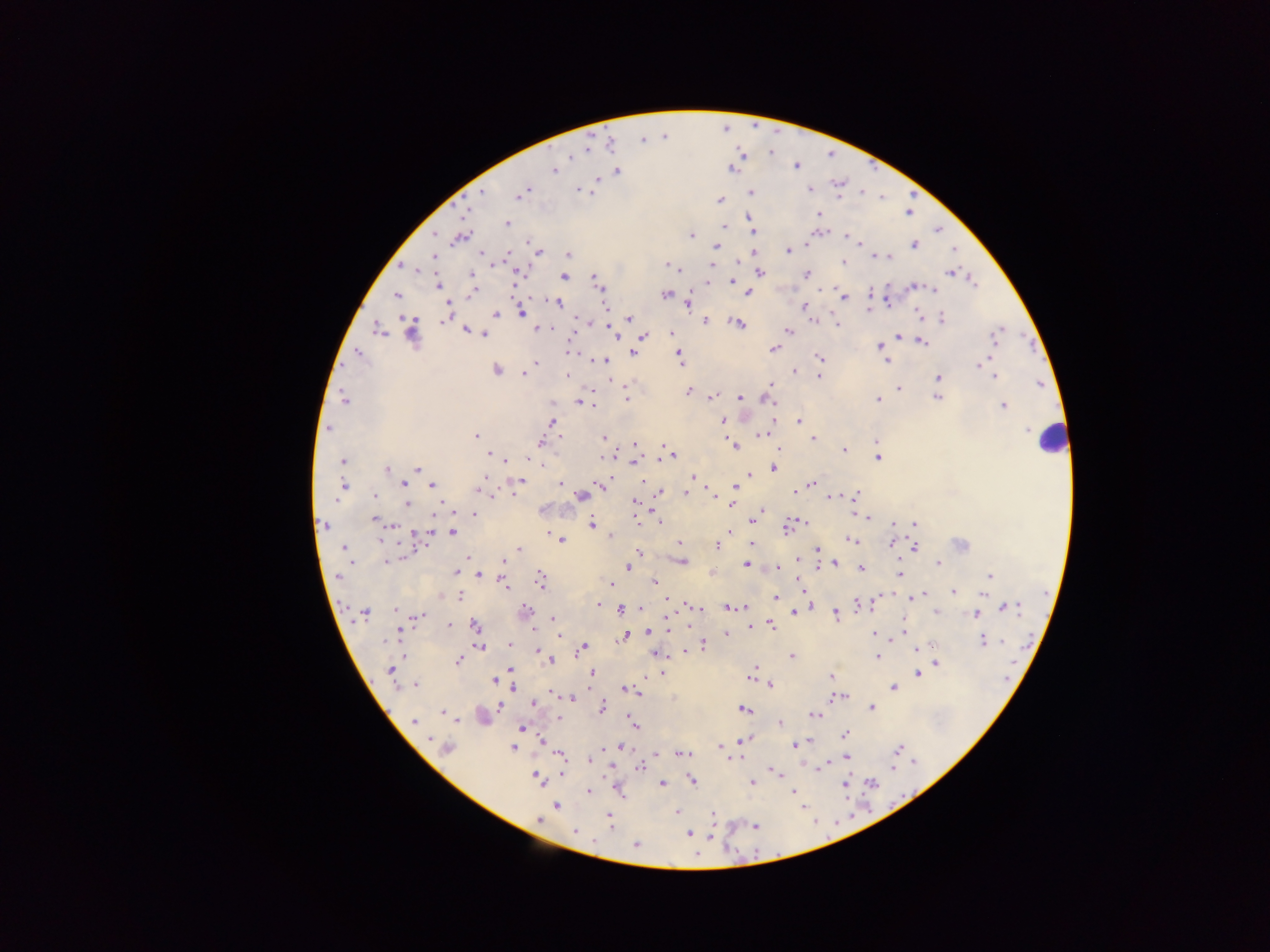

Approximate centers as [x, y] in pixels.
Summary:
  - Plasmodium parasite locations: [755, 126], [726, 127], [664, 136], [643, 139], [609, 144], [588, 146], [737, 147], [831, 152], [774, 154], [746, 156], [796, 164], [868, 166], [554, 169], [731, 169], [616, 170], [598, 178], [837, 188], [578, 189], [810, 189], [481, 192], [522, 192], [750, 192], [590, 193], [910, 193], [881, 196], [719, 200], [464, 210], [909, 210], [819, 213], [747, 217], [508, 224], [751, 224], [939, 226], [726, 227], [722, 231], [433, 234], [691, 235], [845, 235], [813, 236], [459, 237], [861, 243], [914, 244], [715, 246], [787, 250], [954, 251], [538, 252], [480, 253], [754, 253], [507, 255], [567, 255], [434, 256], [877, 256], [881, 257], [888, 257], [736, 259], [844, 262], [668, 265], [404, 266], [711, 266], [673, 268], [519, 273], [759, 273], [949, 273], [472, 274], [806, 274], [593, 275], [563, 276], [972, 280], [707, 281], [733, 282], [438, 285], [913, 286], [823, 287], [600, 289], [932, 289], [472, 292], [748, 292], [666, 294], [397, 295], [510, 296], [869, 296], [886, 296], [843, 297], [558, 301], [688, 303], [803, 307], [916, 307], [446, 310], [496, 313], [521, 313], [446, 318], [630, 318], [940, 318], [920, 319], [581, 320], [705, 320], [813, 320], [833, 320], [736, 323], [837, 324], [536, 328], [548, 328], [377, 329], [1001, 329], [465, 330], [788, 330], [411, 331], [611, 332], [484, 334], [671, 334], [642, 336], [898, 336], [996, 338], [920, 340], [878, 346], [773, 349], [567, 351], [633, 353], [357, 354], [679, 356], [592, 359], [819, 359], [605, 360], [885, 360], [535, 362], [982, 363], [496, 369], [793, 371], [523, 375], [567, 376], [818, 376], [995, 376], [938, 378], [770, 383], [625, 384], [898, 389], [687, 390], [711, 397], [739, 397], [937, 397], [343, 399], [626, 399], [772, 399], [877, 400], [580, 401], [1003, 406], [723, 420], [552, 422], [799, 422], [328, 428], [761, 434], [476, 437], [603, 438], [812, 439], [878, 439], [540, 443], [635, 444], [734, 445], [778, 448], [843, 450], [489, 455], [670, 455], [877, 456], [343, 461], [505, 461], [541, 462], [634, 462], [773, 468], [387, 469], [418, 469], [750, 474], [692, 477], [519, 480], [642, 480], [403, 483], [600, 483], [560, 484], [811, 484], [432, 486], [481, 486], [342, 487], [735, 487], [795, 488], [659, 492], [512, 493], [712, 493], [686, 494], [855, 494], [374, 496], [834, 496], [581, 497], [634, 502], [731, 503], [406, 504], [442, 505], [764, 511], [853, 512], [474, 513], [805, 517], [869, 517], [659, 518], [375, 519], [751, 520], [892, 523], [592, 524], [915, 524], [324, 525], [391, 526], [787, 527], [413, 530], [728, 530], [452, 532], [610, 535], [560, 540], [427, 541], [852, 541], [892, 542], [679, 543], [751, 544], [716, 545], [914, 546], [345, 548], [816, 549], [520, 550], [639, 551], [505, 556], [796, 556], [401, 557], [467, 558], [503, 560], [386, 561], [682, 561], [835, 562], [938, 563], [746, 565], [777, 567], [860, 567], [628, 568], [816, 568], [455, 572], [711, 573], [478, 574], [900, 575], [989, 575], [338, 576], [799, 578], [540, 580], [653, 582], [502, 584], [612, 584], [801, 588], [953, 592], [922, 594], [982, 594], [1046, 594], [879, 595], [440, 596], [459, 596], [805, 597], [908, 597], [775, 598], [667, 599], [598, 605], [857, 605], [693, 606], [809, 606], [1005, 606], [641, 607], [622, 608], [698, 608], [726, 608], [744, 608], [364, 612], [524, 612], [935, 612], [794, 613], [977, 613], [1045, 614], [417, 615], [835, 615], [553, 619], [449, 625], [475, 625], [770, 625], [687, 627], [749, 628], [666, 629], [399, 631], [903, 631], [646, 632], [874, 633], [726, 634], [900, 635], [558, 636], [625, 636], [895, 637], [982, 640], [1003, 640], [510, 644], [702, 644], [479, 645], [1027, 645], [583, 647], [916, 648], [537, 651], [683, 652], [657, 653], [791, 655], [877, 657], [457, 660], [551, 661], [935, 662], [510, 668], [754, 668], [391, 670], [591, 671], [662, 672], [916, 674], [751, 677], [830, 677], [1009, 678], [643, 679], [494, 680], [415, 685], [770, 685], [513, 688], [892, 688], [623, 689], [631, 691], [638, 693], [555, 695], [843, 696], [832, 697], [573, 698], [534, 703], [499, 706], [601, 708], [870, 708], [743, 709], [442, 712], [450, 714], [814, 714], [482, 717], [558, 718], [630, 719], [414, 721], [634, 723], [781, 724], [522, 728], [845, 733], [742, 740], [810, 741], [541, 742], [796, 743], [620, 746], [720, 747], [447, 748], [513, 748], [898, 749], [560, 753], [680, 753], [656, 755], [740, 757], [590, 758], [847, 758], [723, 761], [911, 761], [824, 764], [612, 766], [640, 767], [888, 767], [562, 772], [777, 773], [537, 778], [691, 779], [662, 782], [751, 782], [872, 782], [845, 783], [617, 789], [910, 789], [590, 791], [792, 791], [894, 805], [556, 806], [677, 812], [871, 813], [714, 814], [850, 814], [608, 816], [539, 819], [814, 820], [610, 823], [755, 825], [574, 830], [689, 833], [828, 835], [636, 844], [739, 854], [778, 854]
  - Leukocyte locations: [1052, 439]
  - Field of view: single
  - Capture: mobile-phone photograph through a microscope
  - Preparation: thick blood smear
  - Country: Ghana
  - Image size: 1270×952 pixels